Classify this cell by malaria status.
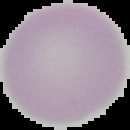
It is uninfected.

Image is 130×130 pixels. Segmented cell region on a black background. From a thin blood smear.